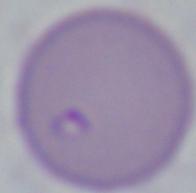
Photomicrograph. A Babesia parasite is shown. 1000x magnification.